State the blood parasite species.
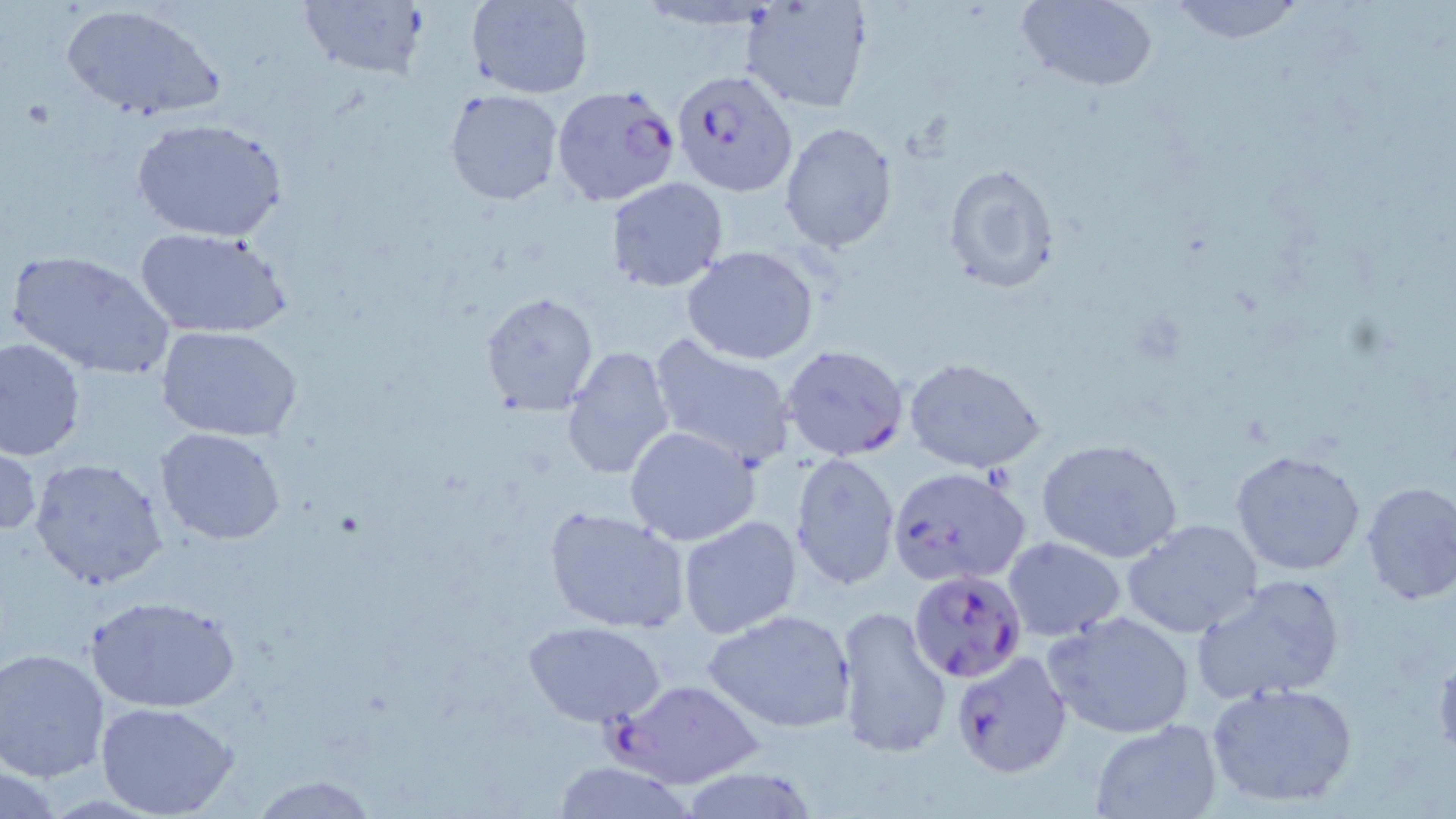

Plasmodium falciparum.

Approximate bounding boxes as (x1,y1)-(x2,y2) corner pairs in pixels. Uninfected red blood cell locations: (467,0)-(593,99), (740,0)-(874,115), (1014,0)-(1158,90), (1164,0)-(1308,43), (296,1)-(429,82), (58,3)-(225,121), (444,89)-(563,206), (132,118)-(289,243), (778,122)-(897,254), (943,164)-(1059,293), (607,178)-(728,291), (135,228)-(291,340), (682,246)-(818,365), (6,249)-(176,382), (478,291)-(599,415), (159,326)-(302,442), (646,333)-(798,469), (0,337)-(86,461), (560,346)-(676,481), (903,356)-(1044,473), (623,426)-(763,548), (155,427)-(287,545), (1037,438)-(1184,563), (0,444)-(43,540), (1230,449)-(1366,576), (790,452)-(901,592), (28,457)-(168,591), (1359,480)-(1456,605), (543,505)-(691,636), (677,515)-(803,639), (1123,517)-(1266,640), (1003,537)-(1125,639), (1191,574)-(1346,706), (86,595)-(241,713), (832,604)-(952,760), (701,608)-(857,735), (1043,610)-(1197,740), (525,621)-(666,727), (1,647)-(114,783), (1207,681)-(1359,809), (96,702)-(239,818), (1090,720)-(1222,817), (548,761)-(701,818), (1,762)-(64,818), (253,775)-(376,817). Plasmodium falciparum-infected red blood cell locations: (671,67)-(798,196), (550,85)-(681,207), (780,343)-(910,462), (886,464)-(1032,588), (907,568)-(1027,682), (949,650)-(1075,778), (611,677)-(764,790). Image is 1456×819 pixels. Thin blood film. Optical microscopy. May-Grünwald-Giemsa-stained preparation. One field of a larger specimen. Captured at 1000x magnification.